Name the parasite shown.
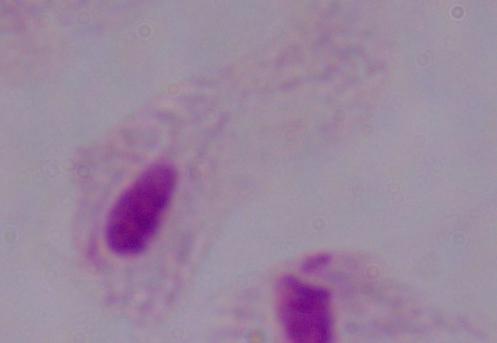
A trichomonad.

modality = micrograph
magnification = 1000x